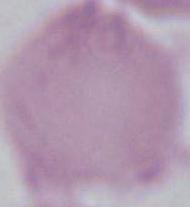
{
  "identification": "erythrocyte",
  "magnification": "1000x",
  "modality": "micrograph"
}